Mark where platelets are.
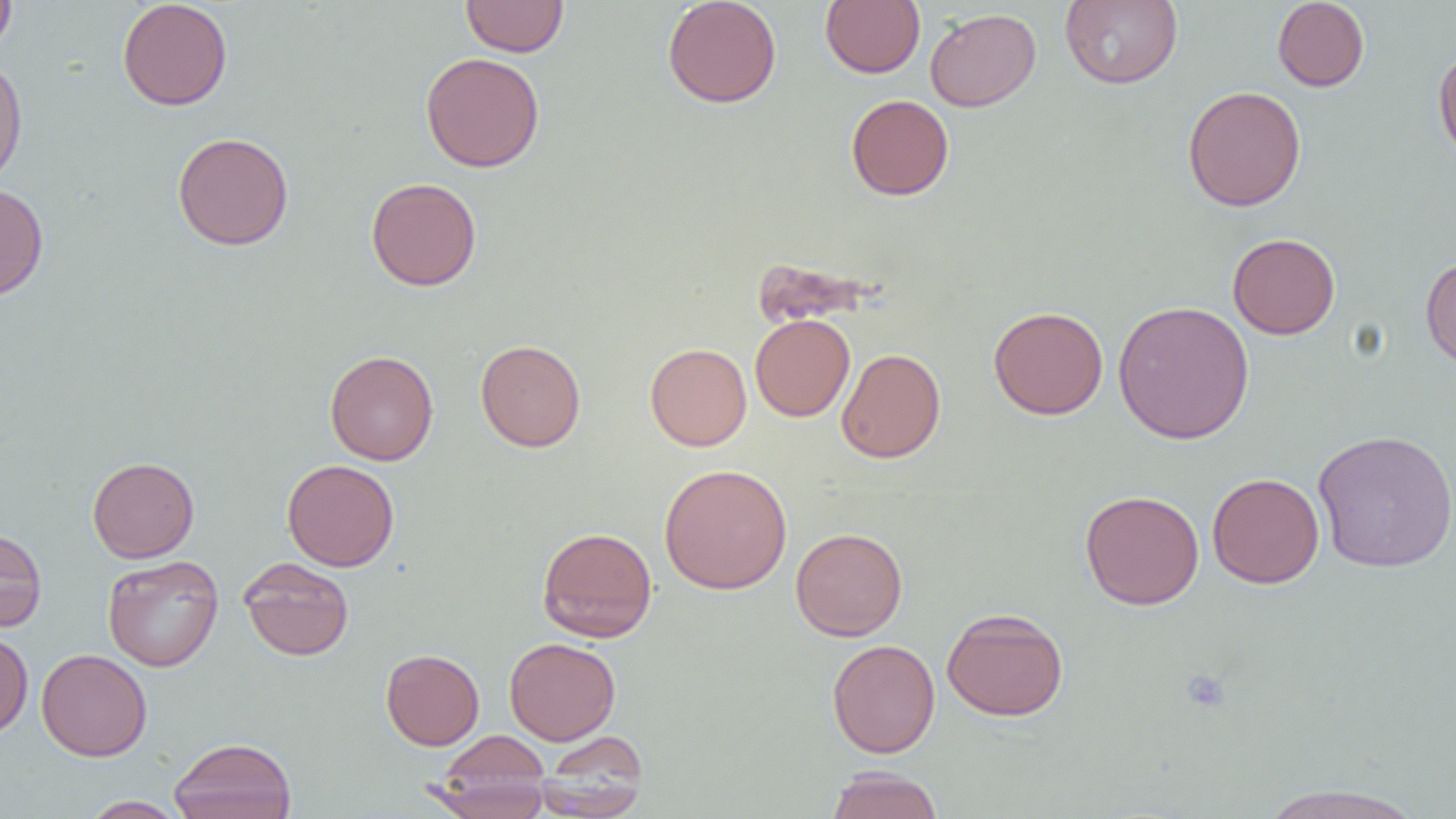

Approximate bounding boxes as (x1,y1)-(x2,y2) corner pairs in pixels.
Platelets: (1181,668)-(1231,714).

slide-level diagnosis = no evidence of blood parasites
modality = light microscopy
field of view = single
uninfected red blood cell locations = approximate bounding boxes as (x1,y1)-(x2,y2) corner pairs in pixels: (0,0)-(17,57), (117,0)-(233,111), (461,0)-(569,57), (662,0)-(782,108), (820,0)-(925,77), (1060,0)-(1183,89), (1272,0)-(1370,91), (925,7)-(1041,112), (1433,43)-(1456,165), (420,52)-(545,172), (0,59)-(27,190), (1183,85)-(1306,212), (846,94)-(954,200), (172,132)-(294,251), (366,176)-(482,290), (0,183)-(49,301), (1227,233)-(1341,339), (1420,256)-(1456,371), (1113,300)-(1254,444), (988,306)-(1108,419), (750,314)-(855,422), (475,339)-(586,452), (645,343)-(752,451), (836,348)-(946,463), (324,350)-(439,465), (1313,429)-(1456,573), (87,456)-(200,563), (282,459)-(399,571), (659,463)-(792,595), (1207,472)-(1324,588), (1079,490)-(1204,610), (536,526)-(657,642), (0,527)-(47,632), (790,527)-(908,641), (103,555)-(223,672), (238,557)-(354,661), (942,607)-(1069,720), (0,629)-(33,738), (504,637)-(620,745), (827,639)-(940,758), (36,648)-(152,761), (380,649)-(484,750), (536,729)-(649,813), (434,731)-(552,803), (168,737)-(297,819), (826,766)-(944,819), (427,767)-(551,819), (1257,784)-(1427,819), (79,796)-(188,818)
preparation = thin blood film
magnification = 1000x
image size = 1456×819 pixels